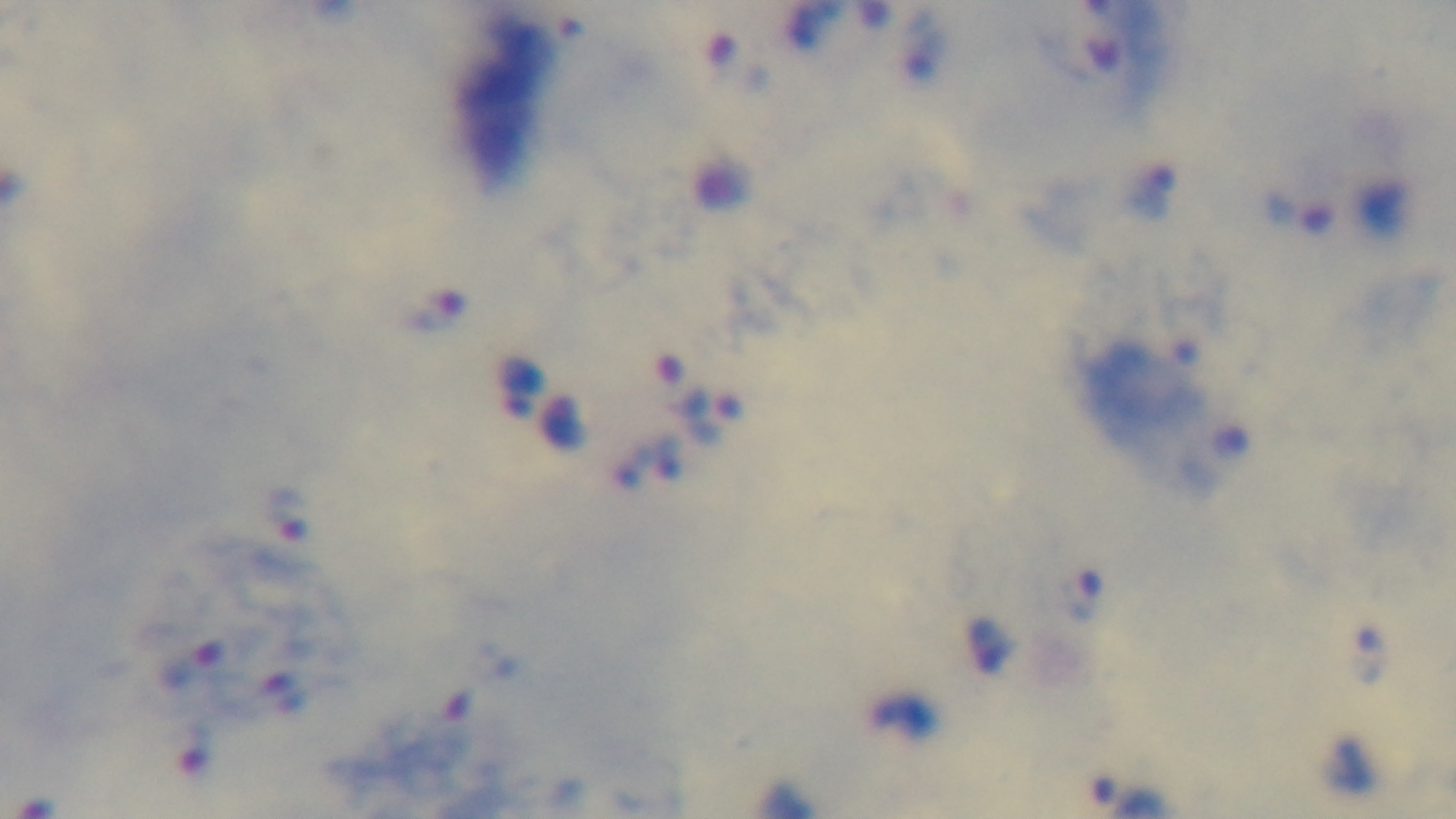 Preparation: thick. Malaria status: positive. Photomicrograph. Single field of view. Captured with a mounted 4K digital camera. Giemsa-stained. Oil-immersion objective, 100x.